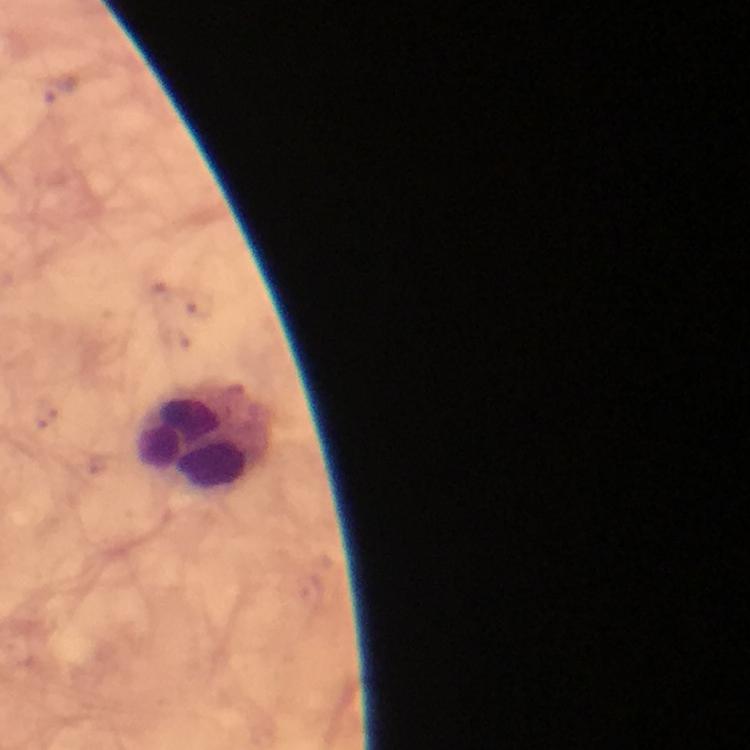
Approximate centers as {x, y} in pixels.
Summary:
  - Leukocyte locations: {205, 435}
  - Immersion oil: applied
  - Magnification: 100x
  - Capture: smartphone photograph through a microscope
  - Stain: Giemsa
  - Context: from a malaria diagnostic workup
  - Cropped from: a single field of view
  - Plasmodium parasites: none seen
  - Preparation: thick blood smear
  - Image size: 750×750 pixels